Assess the morphology of the erythrocytes.
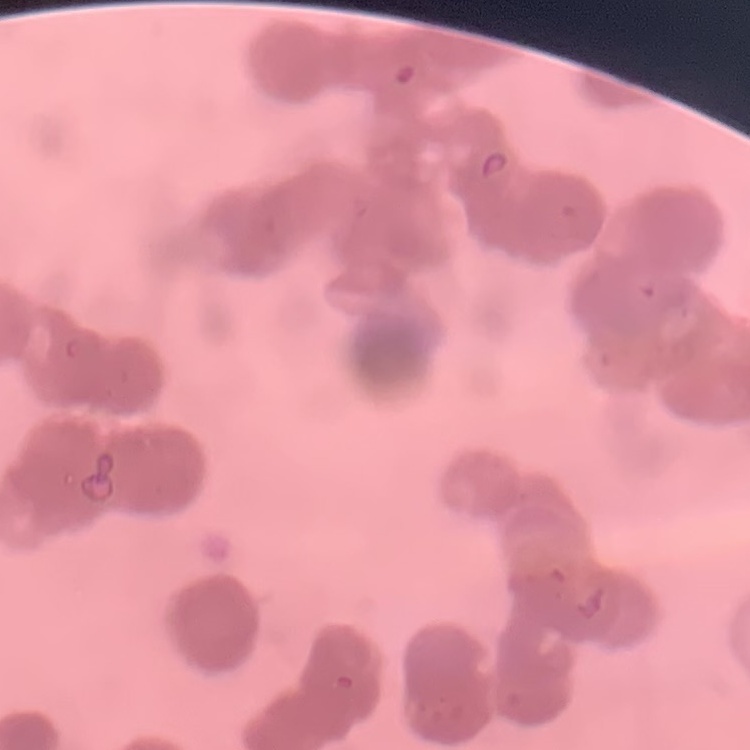

Rouleaux formation.

Summary:
  - Preparation: thin blood film
  - Stain: Field's or Giemsa
  - Image type: square crop of a larger photomicrograph